Classify this cell by malaria status.
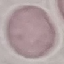

It is uninfected.

image type = cell patch, automatically extracted from a larger field of view and resized to 64 × 64 pixels
capture = smartphone through the microscope eyepiece
preparation = thin blood film
stain = Giemsa